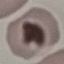
malaria status = uninfected
stain = Giemsa
image type = cell patch, automatically extracted from a larger field of view and resized to 64 × 64 pixels
capture = smartphone through the microscope eyepiece
preparation = thin blood smear